Classify this cell by malaria status.
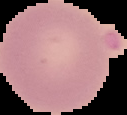
It is uninfected.

Summary:
  - Preparation: thin blood smear
  - Image size: 127×115 pixels
  - Image type: segmented cell region with the area outside set to black